Assess for malaria.
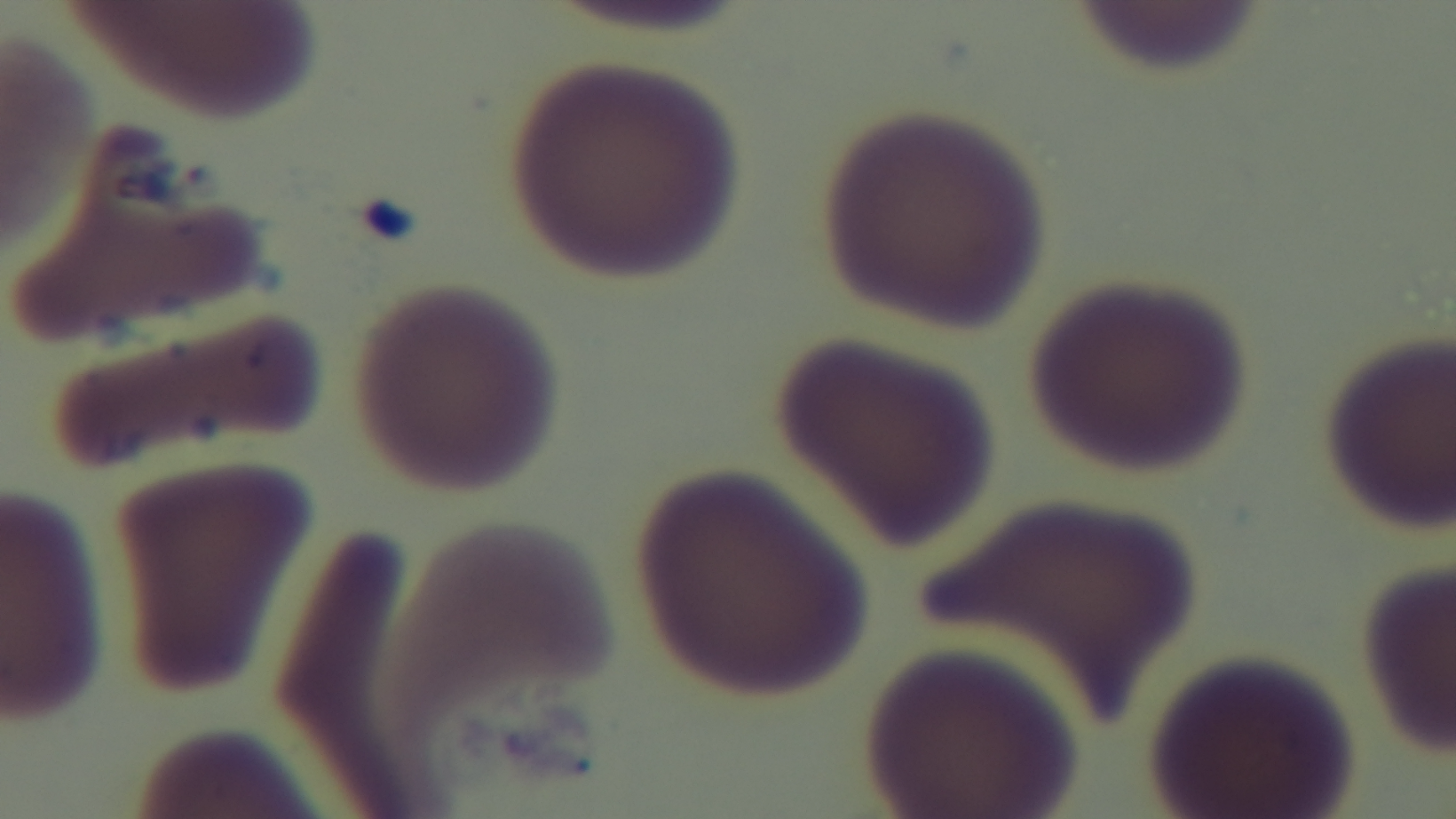

Negative.

objective = 100x oil immersion
preparation = thin smear
field of view = one from the slide
capture = mounted 4K digital camera
stain = Giemsa
modality = light microscopy